Assess this cell for malaria.
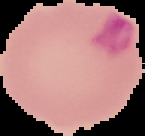

It is parasitized.

Summary:
  - Preparation: thin blood film
  - Image type: cell region segmented out of the field of view; surrounding area masked to black
  - Image size: 145×136 pixels